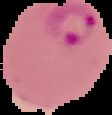

Segmented cell region on a black background. Result: malaria parasites detected. Image is 112×115 pixels. From a thin blood smear.